Comment on the morphology of the red blood cells.
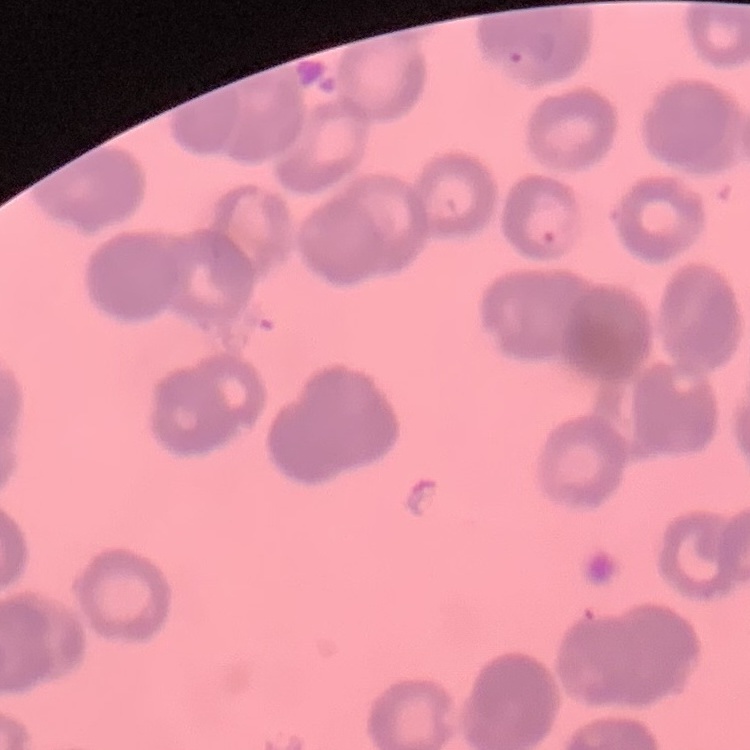
They show rouleaux formation.

Summary:
  - Preparation: thin blood film
  - Stain: Field's or Giemsa
  - Image type: square crop of a larger photomicrograph